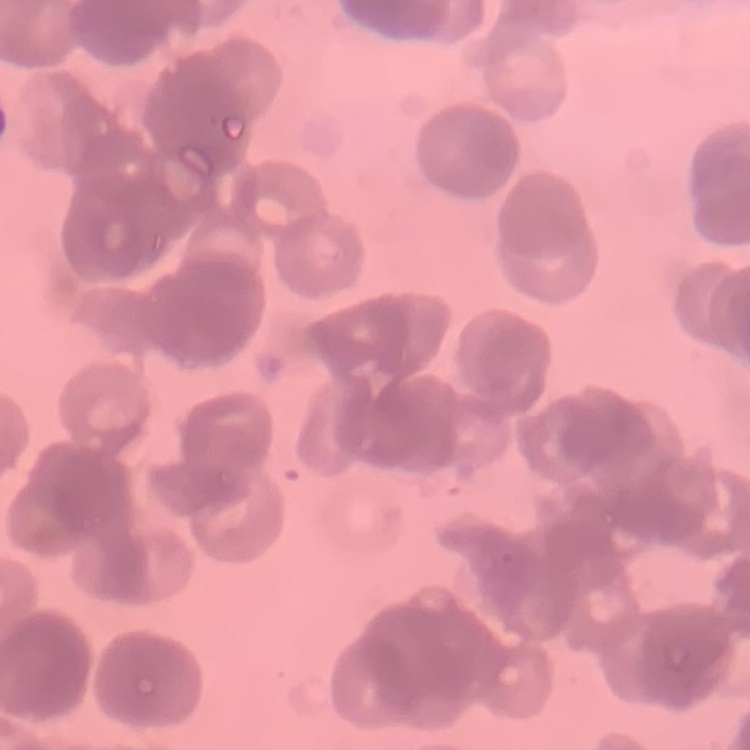
The red blood cells show rouleaux formation. Square crop of a larger photomicrograph. Thin peripheral smear. Stained with either Field's or Giemsa.